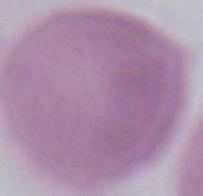

1000x magnification. Photomicrograph. An erythrocyte is seen.